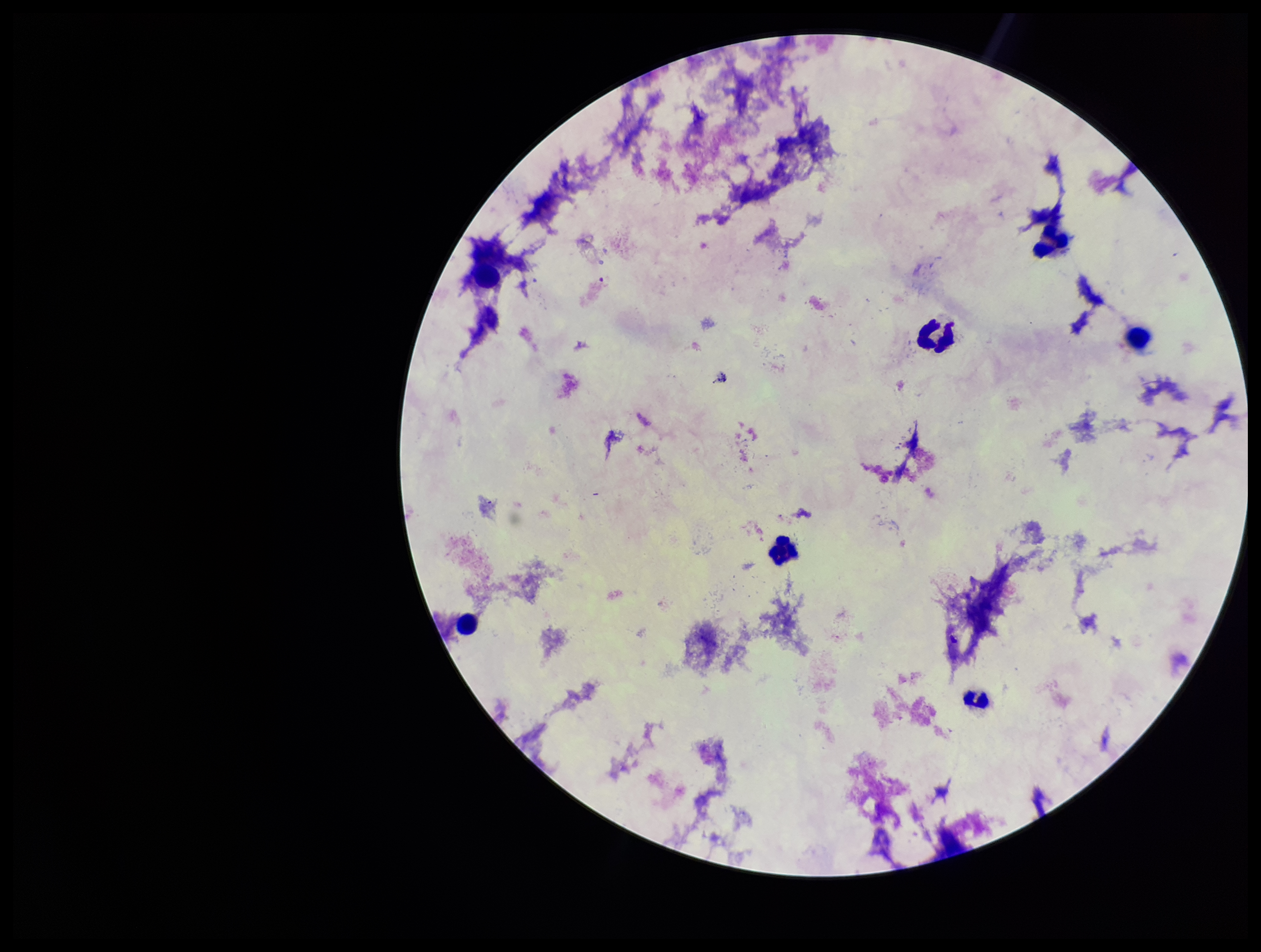
Summary:
  - Parasite count: 0
  - Field of view: one from this slide
  - Plasmodium parasites: none seen
  - Preparation: thick blood smear
  - Image size: 1261×952 pixels
  - Stain: Giemsa
  - Patient malaria status: negative
  - Leukocyte count: 6
  - Capture: smartphone photograph through the microscope eyepiece